Report the malaria status of this cell.
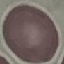
It is uninfected.

{
  "preparation": "thin smear",
  "image_type": "automatically extracted cell patch, resized to 64 × 64 pixels",
  "stain": "Giemsa",
  "capture": "smartphone through the microscope eyepiece"
}